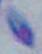 Micrograph. 1000x magnification. Toxoplasma gondii is seen.